Assess this cell for malaria.
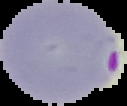
It is parasitized.

image size = 127×106 pixels
image type = segmented cell region with the area outside set to black
preparation = thin blood smear